Name the parasite shown.
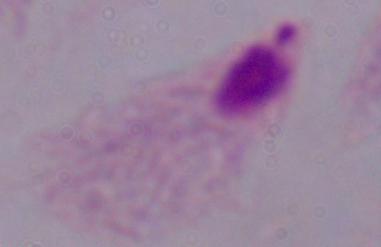
A trichomonad.

Summary:
  - Modality: photomicrograph
  - Magnification: 1000x